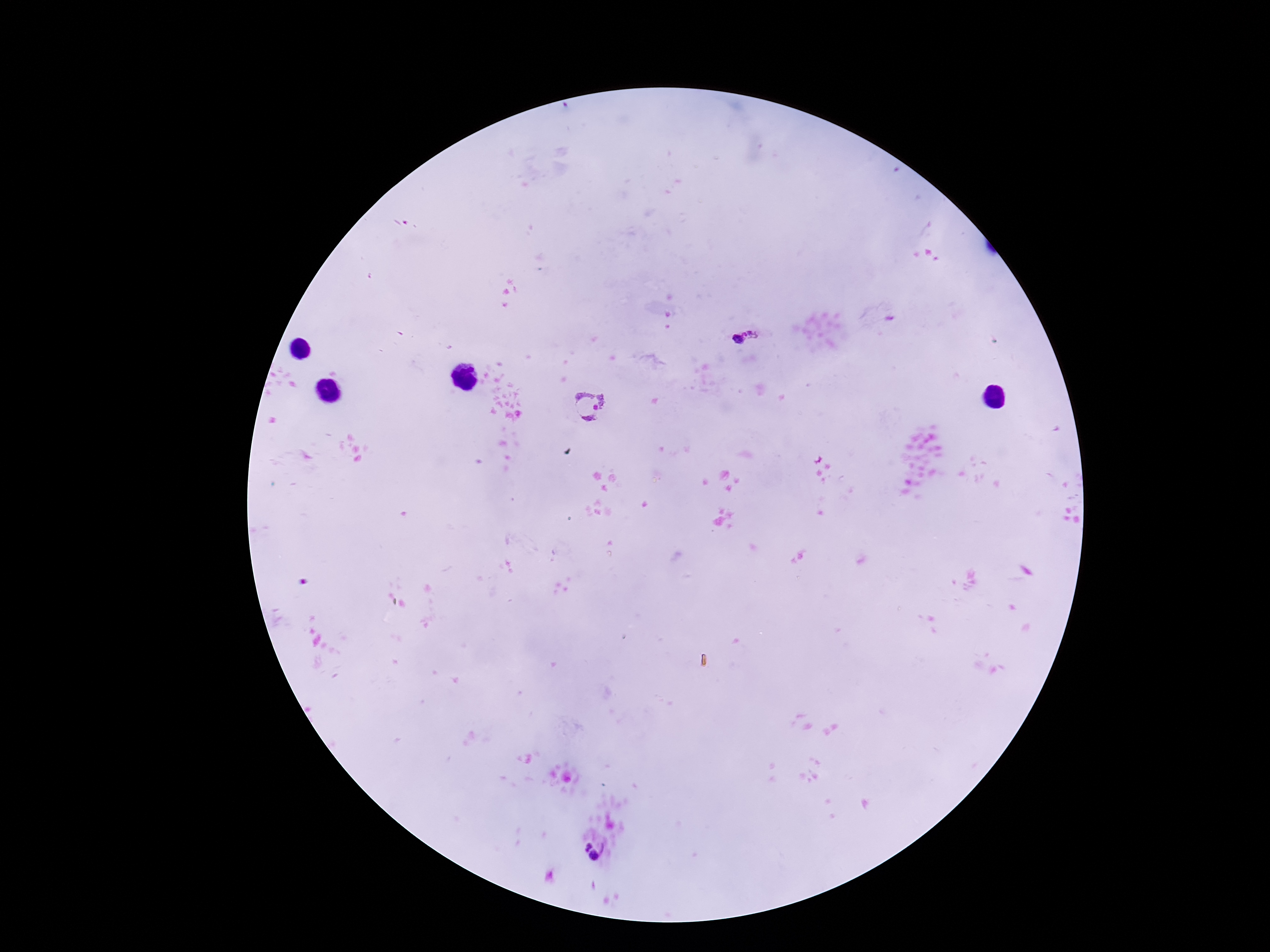

stain = Giemsa
magnification = 100x
field of view = one from this slide
Plasmodium parasite locations = approximate centers as {x, y} in pixels: {746, 335}, {590, 406}, {582, 843}, {596, 857}
image size = 1270×952 pixels
patient malaria status = positive
preparation = thick blood smear
capture = smartphone camera through the microscope eyepiece